Report the malaria status of this cell.
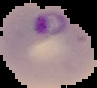

Parasitized.

Image is 97×88 pixels. The area outside the segmented cell region is set to black. From a thin blood smear.